State which parasite is depicted.
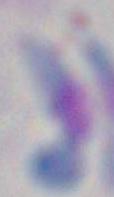
This is Toxoplasma gondii.

{
  "magnification": "1000x",
  "modality": "photomicrograph"
}